Locate leukocytes (white blood cells).
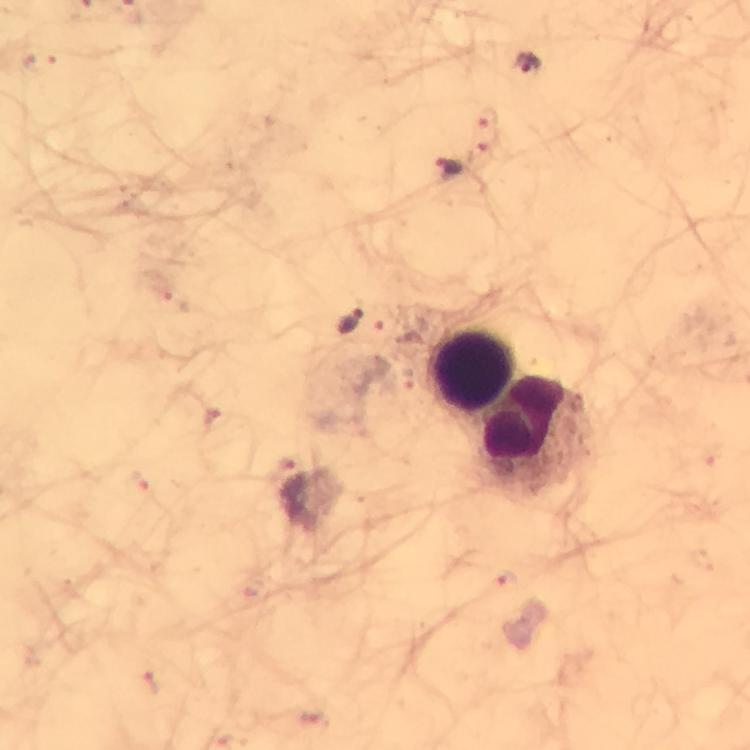

Approximate object centers, in pixels from the top-left corner.
Leukocytes: (x=474, y=370), (x=538, y=426).

Plasmodium parasite locations: (x=528, y=64), (x=450, y=169), (x=351, y=324). A crop from one field of view. Image is 750×750 pixels. Giemsa stain. Smartphone photograph taken through a microscope. Immersion oil applied. Thick blood film. 100x magnification. From a diagnostic examination for malaria.